Mark where platelets are.
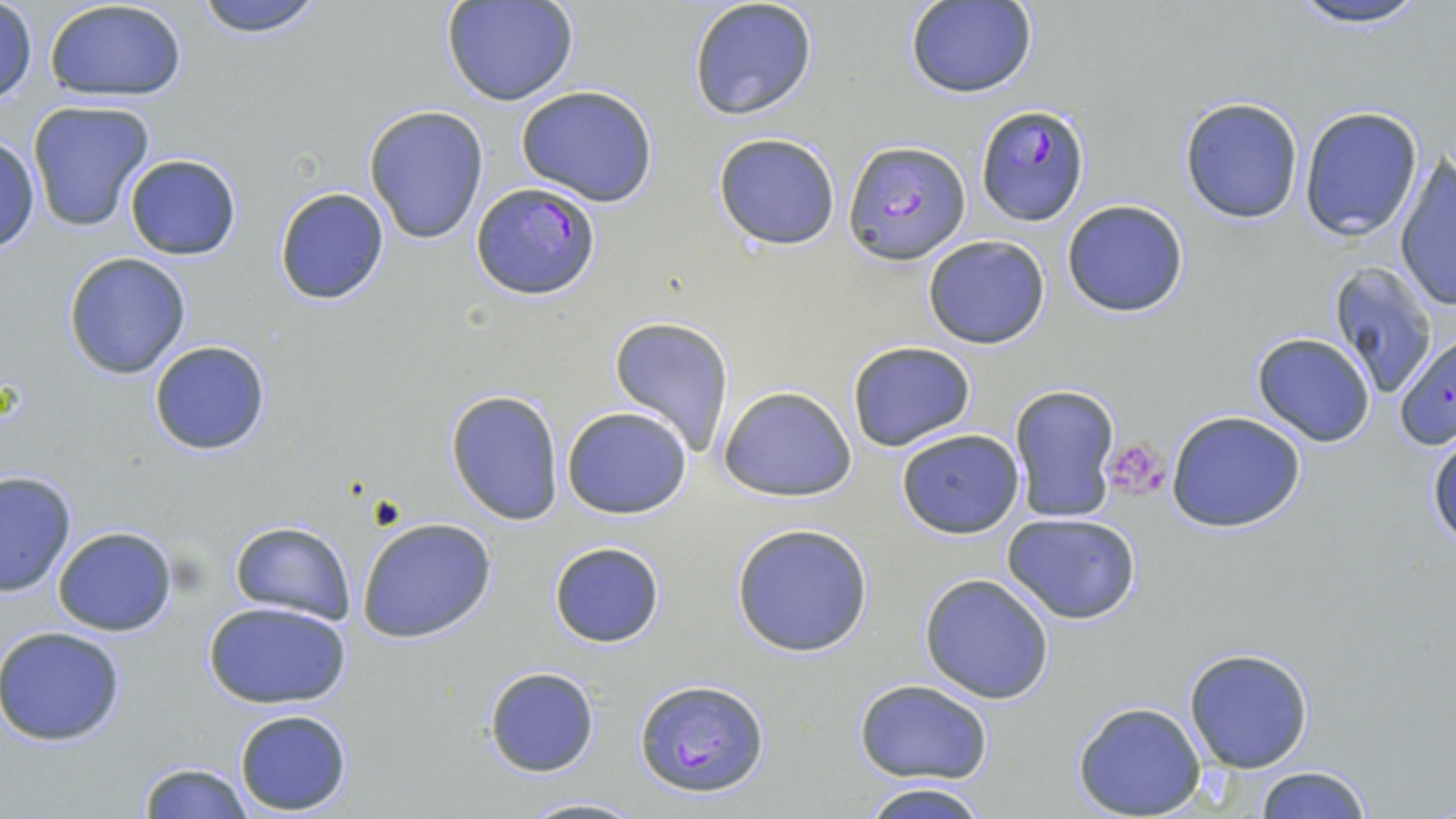

Approximate bounding boxes as [x1, y1, x2, y2] in pixels.
Platelets: [1100, 438, 1169, 501].

Plasmodium falciparum-infected red blood cell locations: [976, 105, 1090, 227], [843, 140, 972, 266], [470, 183, 601, 300], [1393, 332, 1455, 453], [633, 677, 772, 798]. Uninfected red blood cell locations: [43, 0, 190, 103], [191, 0, 327, 39], [442, 0, 581, 107], [687, 0, 819, 121], [903, 0, 1038, 99], [1279, 0, 1439, 30], [1, 3, 37, 106], [514, 84, 661, 207], [1179, 96, 1306, 224], [26, 99, 158, 233], [364, 106, 490, 246], [1297, 106, 1423, 241], [712, 132, 841, 251], [0, 136, 40, 254], [122, 152, 242, 261], [1393, 156, 1456, 311], [272, 186, 391, 307], [1060, 200, 1189, 318], [923, 235, 1051, 350], [63, 252, 192, 380], [1327, 262, 1440, 398], [609, 315, 733, 458], [1251, 332, 1376, 448], [148, 340, 270, 457], [846, 340, 978, 453], [1009, 384, 1121, 522], [715, 386, 858, 503], [445, 389, 565, 525], [560, 406, 693, 518], [1166, 411, 1308, 533], [894, 427, 1025, 538], [1426, 429, 1456, 549], [1, 470, 76, 596], [1003, 513, 1141, 625], [356, 517, 497, 644], [228, 520, 356, 624], [729, 523, 874, 658], [52, 526, 178, 636], [547, 540, 665, 647], [918, 572, 1057, 704], [203, 602, 350, 709], [0, 626, 127, 746], [1183, 646, 1314, 773], [483, 666, 600, 777], [855, 680, 992, 783], [1072, 701, 1208, 818], [234, 709, 352, 814], [135, 761, 252, 818], [1255, 765, 1372, 819], [856, 781, 994, 819], [515, 793, 644, 818]. Slide-level diagnosis: Plasmodium falciparum. May-Grünwald-Giemsa-stained preparation. Thin blood smear. Optical microscopy. One field of a larger specimen. 1000x magnification. Image is 1456×819 pixels.